Classify this cell by malaria status.
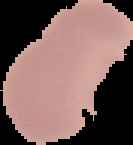

Uninfected.

Cell region segmented out of the field of view; the surrounding area is masked to black. Image is 133×145 pixels. From a thin blood film.